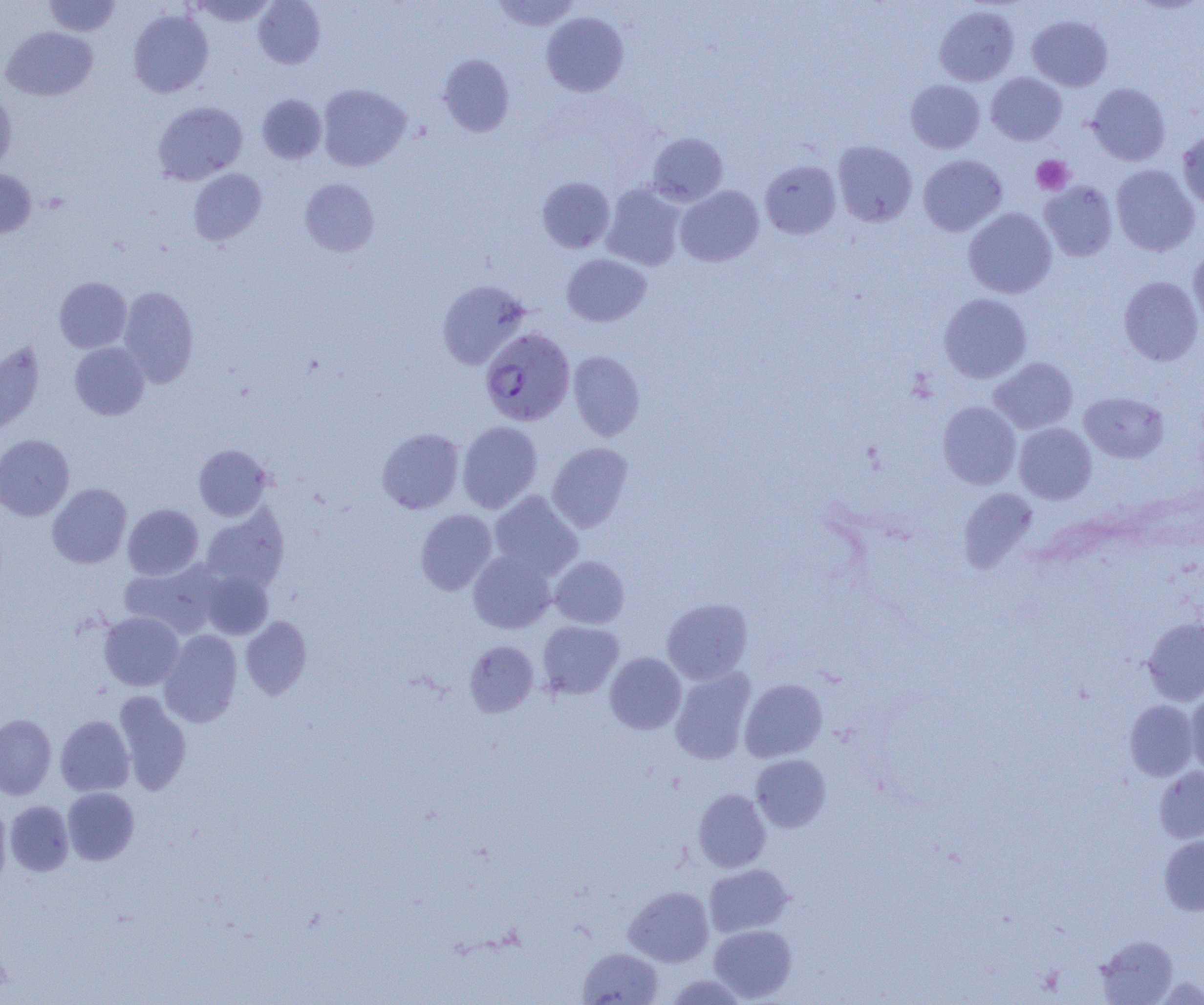

Summary:
  - Coordinate format: approximate bounding boxes as named x1/y1/x2/y2 corners in pixels
  - Uninfected red blood cell locations: (x1=44, y1=0, x2=120, y2=36), (x1=189, y1=0, x2=275, y2=26), (x1=253, y1=0, x2=325, y2=69), (x1=492, y1=0, x2=580, y2=32), (x1=934, y1=5, x2=1019, y2=86), (x1=128, y1=9, x2=213, y2=98), (x1=541, y1=12, x2=629, y2=96), (x1=1027, y1=15, x2=1113, y2=91), (x1=1, y1=26, x2=98, y2=101), (x1=438, y1=54, x2=514, y2=136), (x1=986, y1=72, x2=1067, y2=145), (x1=905, y1=79, x2=985, y2=153), (x1=1086, y1=83, x2=1171, y2=165), (x1=318, y1=84, x2=411, y2=171), (x1=0, y1=90, x2=16, y2=173), (x1=256, y1=94, x2=327, y2=163), (x1=153, y1=101, x2=247, y2=185), (x1=1177, y1=131, x2=1204, y2=210), (x1=647, y1=132, x2=728, y2=206), (x1=833, y1=140, x2=917, y2=227), (x1=918, y1=154, x2=1007, y2=236), (x1=760, y1=159, x2=842, y2=239), (x1=1110, y1=164, x2=1200, y2=257), (x1=0, y1=168, x2=36, y2=238), (x1=188, y1=168, x2=266, y2=245), (x1=536, y1=177, x2=615, y2=253), (x1=300, y1=179, x2=379, y2=256), (x1=1040, y1=180, x2=1118, y2=262), (x1=602, y1=183, x2=685, y2=271), (x1=676, y1=185, x2=764, y2=267), (x1=963, y1=207, x2=1057, y2=298), (x1=1188, y1=246, x2=1204, y2=332), (x1=561, y1=253, x2=651, y2=327), (x1=1118, y1=275, x2=1204, y2=366), (x1=54, y1=277, x2=131, y2=352), (x1=437, y1=281, x2=530, y2=369), (x1=117, y1=286, x2=198, y2=387), (x1=938, y1=293, x2=1032, y2=384), (x1=0, y1=342, x2=44, y2=435), (x1=70, y1=342, x2=149, y2=420), (x1=568, y1=351, x2=645, y2=441), (x1=988, y1=357, x2=1078, y2=434), (x1=1079, y1=390, x2=1169, y2=463), (x1=937, y1=401, x2=1021, y2=489), (x1=457, y1=421, x2=543, y2=513), (x1=1014, y1=422, x2=1097, y2=504), (x1=377, y1=428, x2=464, y2=514), (x1=0, y1=434, x2=74, y2=521), (x1=547, y1=442, x2=634, y2=532), (x1=194, y1=444, x2=272, y2=521), (x1=47, y1=483, x2=132, y2=568), (x1=958, y1=488, x2=1038, y2=573), (x1=489, y1=491, x2=583, y2=580), (x1=123, y1=504, x2=203, y2=580), (x1=200, y1=506, x2=289, y2=592), (x1=415, y1=509, x2=497, y2=595), (x1=468, y1=550, x2=557, y2=633), (x1=550, y1=555, x2=629, y2=628), (x1=119, y1=560, x2=224, y2=638), (x1=201, y1=570, x2=273, y2=639), (x1=662, y1=598, x2=753, y2=684), (x1=99, y1=612, x2=183, y2=690), (x1=241, y1=616, x2=311, y2=700), (x1=1142, y1=616, x2=1204, y2=705), (x1=537, y1=621, x2=624, y2=699), (x1=159, y1=630, x2=242, y2=727), (x1=465, y1=641, x2=539, y2=717), (x1=605, y1=652, x2=686, y2=734), (x1=670, y1=667, x2=756, y2=764), (x1=740, y1=678, x2=828, y2=763), (x1=1185, y1=689, x2=1204, y2=776), (x1=113, y1=691, x2=192, y2=794), (x1=1124, y1=700, x2=1199, y2=781), (x1=0, y1=714, x2=56, y2=799), (x1=55, y1=715, x2=134, y2=796), (x1=751, y1=754, x2=831, y2=832), (x1=1154, y1=767, x2=1204, y2=844), (x1=62, y1=787, x2=139, y2=865), (x1=693, y1=788, x2=771, y2=872), (x1=5, y1=801, x2=74, y2=875), (x1=0, y1=803, x2=11, y2=886), (x1=1159, y1=834, x2=1204, y2=915), (x1=704, y1=864, x2=792, y2=937), (x1=624, y1=886, x2=714, y2=966), (x1=710, y1=924, x2=797, y2=1002), (x1=1095, y1=935, x2=1178, y2=1004), (x1=578, y1=947, x2=664, y2=1005), (x1=663, y1=974, x2=751, y2=1005)
  - Plasmodium falciparum-infected red blood cell locations: (x1=480, y1=328, x2=575, y2=426)
  - Platelet locations: (x1=1032, y1=155, x2=1073, y2=195)
  - Slide-level diagnosis: Plasmodium falciparum
  - Field of view: one of a larger specimen
  - Image size: 1204×1005 pixels
  - Modality: light microscopy
  - Preparation: thin blood smear
  - Magnification: 1000x